Point out each leukocyte.
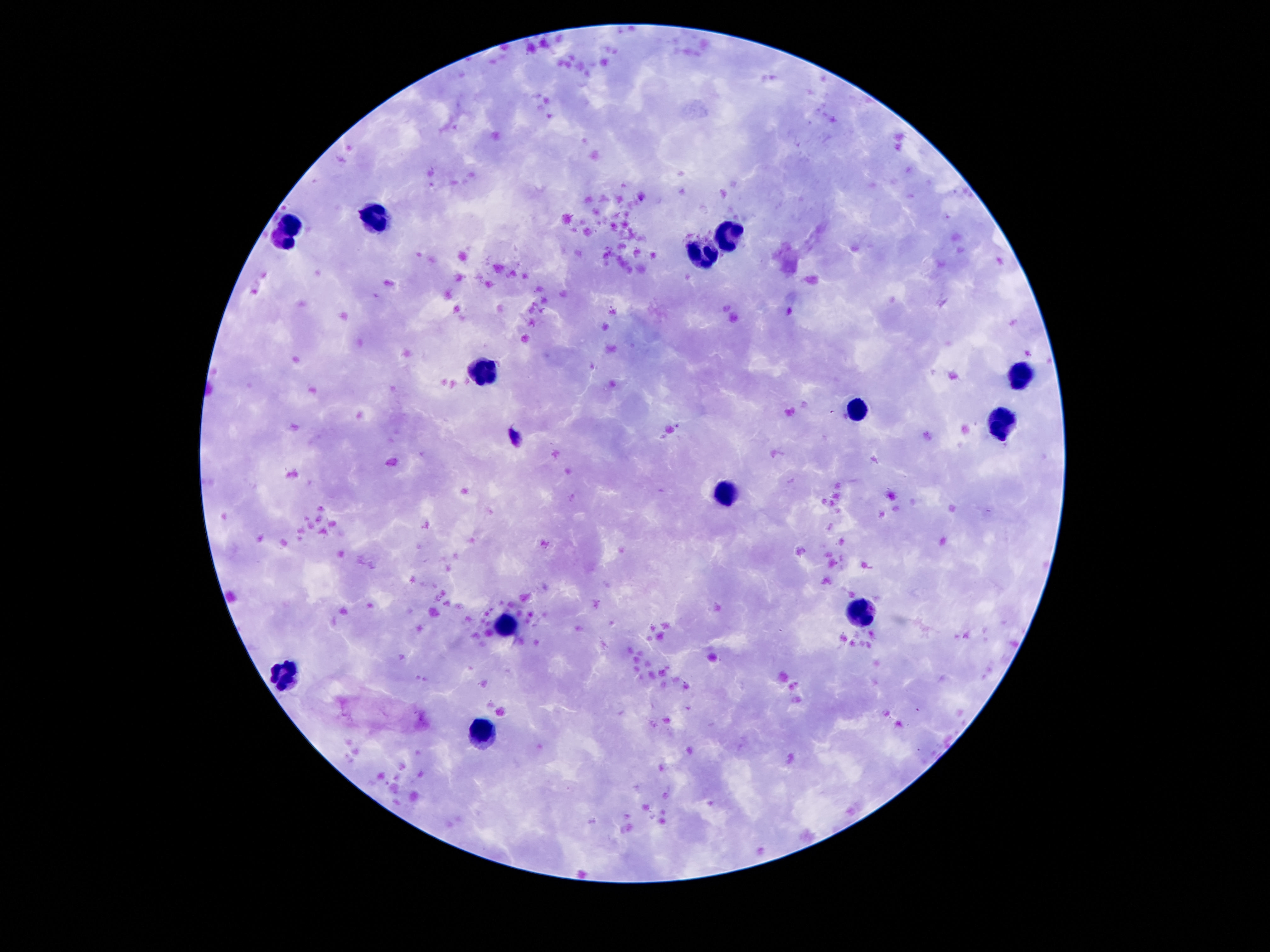

Approximate centers as {x, y} in pixels.
Leukocytes: {374, 219}, {288, 233}, {729, 235}, {705, 252}, {488, 370}, {1020, 375}, {855, 410}, {999, 424}, {726, 492}, {864, 613}, {503, 623}, {285, 676}, {482, 732}.

{
  "capture": "smartphone camera through the microscope eyepiece",
  "patient_malaria_status": "negative",
  "preparation": "thick peripheral-blood smear",
  "stain": "Giemsa",
  "magnification": "100x",
  "field_of_view": "single",
  "image_size": "1270×952 pixels"
}